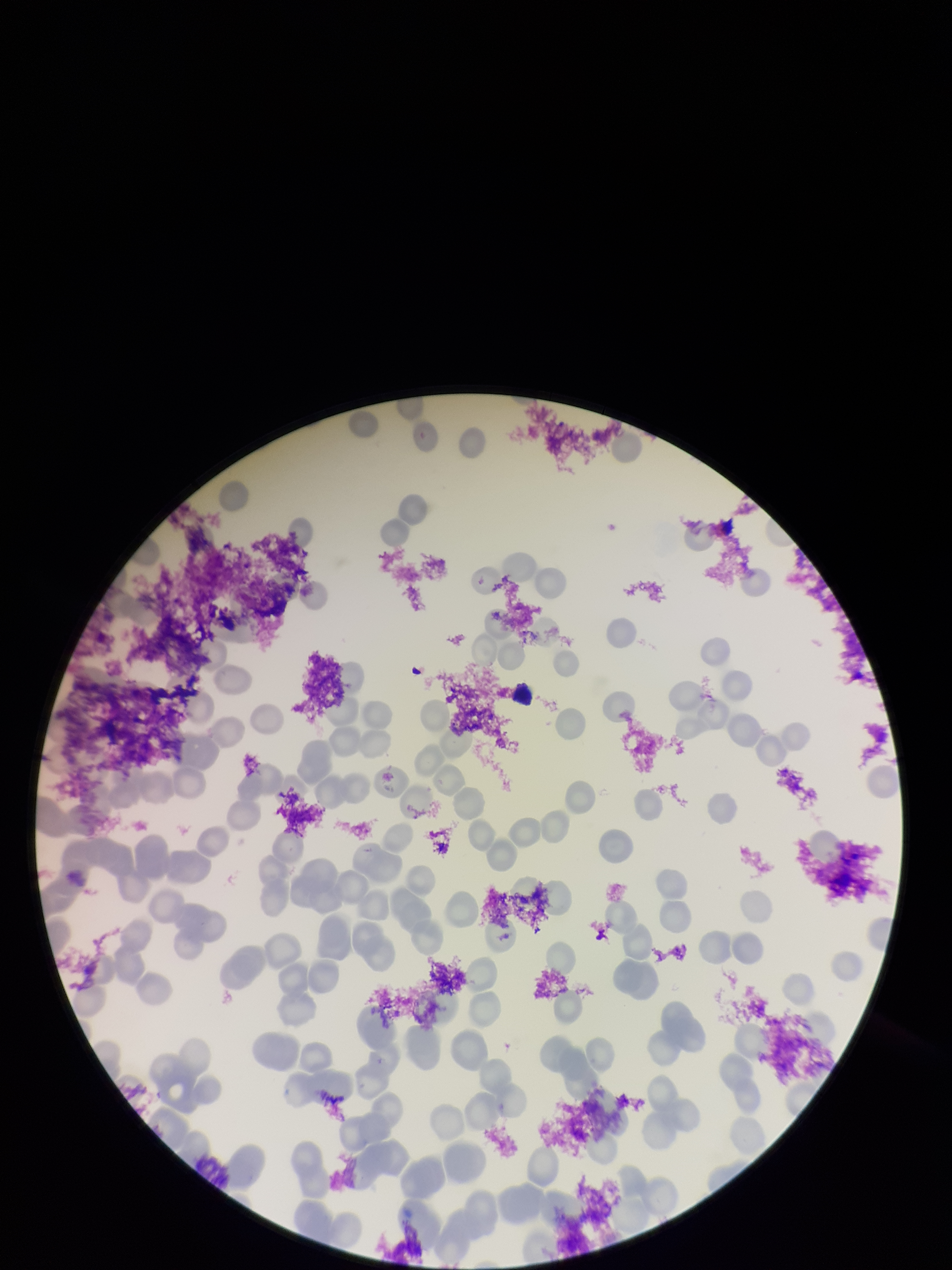

Summary:
  - Parasitized red blood cells: none seen
  - Preparation: thin smear
  - Stain: Giemsa
  - Image size: 952×1270 pixels
  - Parasitized red blood cell count: 0
  - Field of view: single
  - Capture: smartphone photograph through the microscope eyepiece
  - Patient malaria status: positive
  - Red blood cell count: 157
  - Species reported for this patient: Plasmodium falciparum